Describe the morphology of the red blood cells.
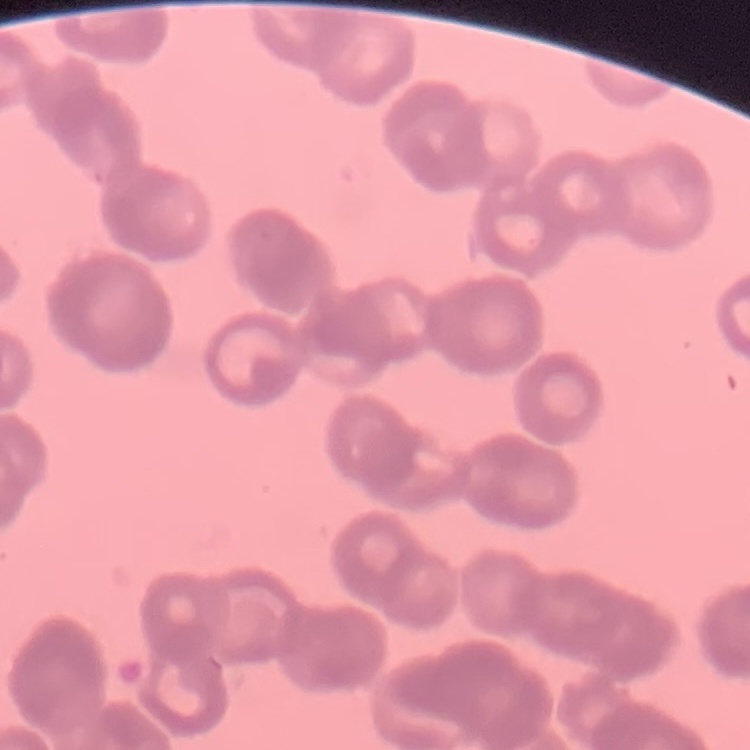

They show rouleaux formation.

Thin peripheral smear. Square crop of a larger photomicrograph. Field's or Giemsa stain.